Name the parasite shown.
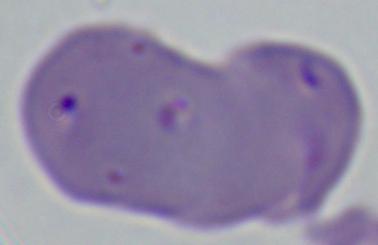

Babesia.

Micrograph. Captured at 1000x magnification.